Report the malaria status of this cell.
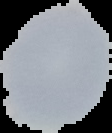

It is uninfected.

Summary:
  - Image type: segmented cell region with the area outside set to black
  - Image size: 112×133 pixels
  - Preparation: thin blood smear